Report the malaria status of this cell.
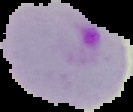

Parasitized.

From a thin blood smear. Image is 133×112 pixels. Segmented cell region on a black background.